Identify the cell.
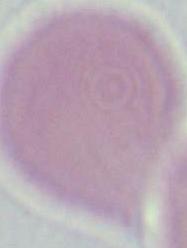
This is an erythrocyte.

Micrograph. Captured at 1000x magnification.